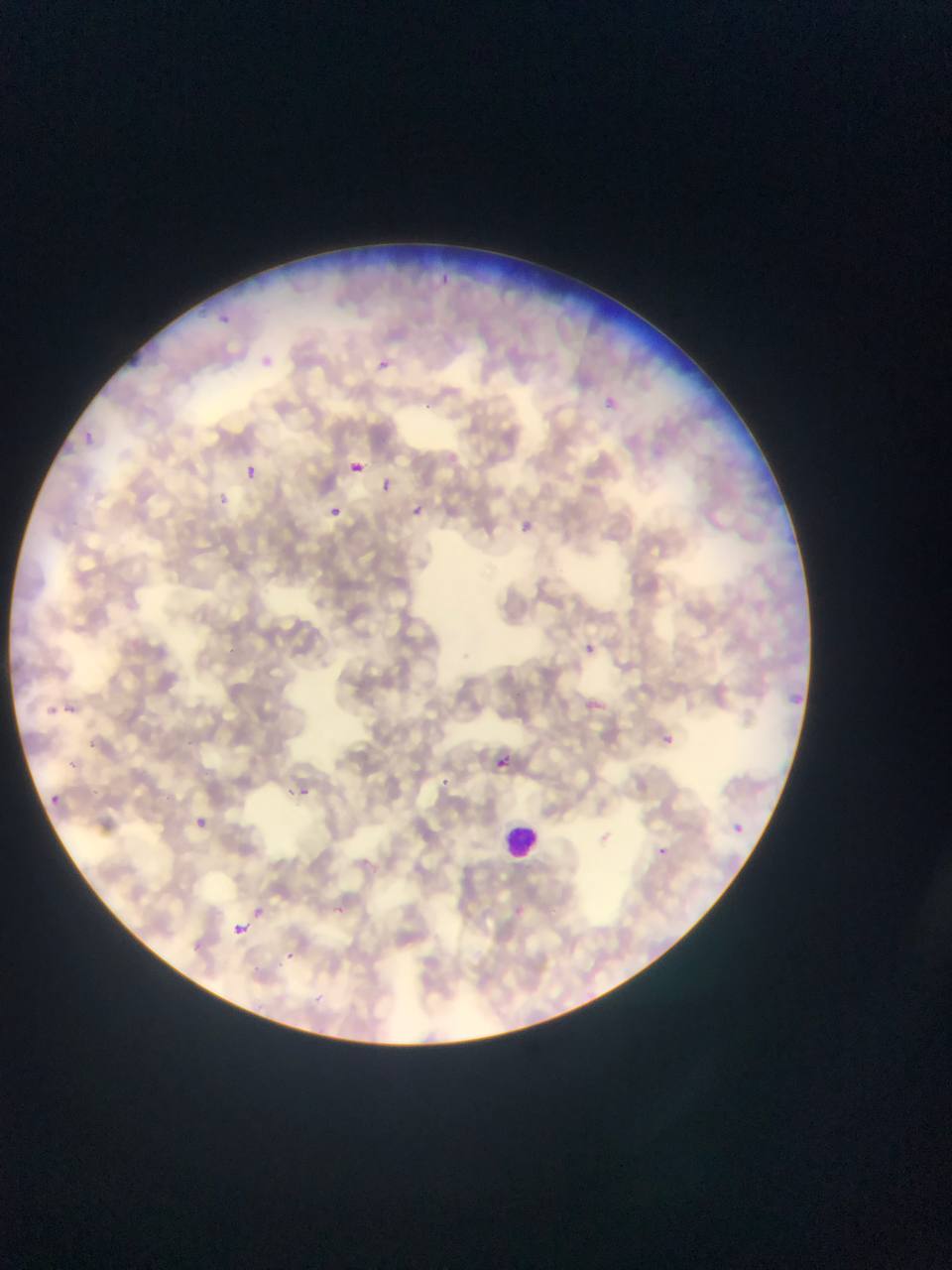
Approximate bounding boxes as (left, top, right, bottom) in pixels. Leukocyte locations: (499, 820, 535, 860). Malaria parasite locations: (426, 273, 462, 291), (219, 313, 230, 323), (258, 342, 298, 375), (126, 347, 149, 373), (377, 359, 390, 370), (600, 390, 617, 411), (83, 437, 91, 449), (345, 448, 362, 471), (245, 465, 258, 479), (375, 468, 403, 501), (202, 486, 233, 507), (400, 501, 440, 529), (509, 503, 540, 539), (331, 507, 340, 517), (577, 628, 600, 678), (785, 681, 808, 707), (48, 706, 58, 713), (650, 719, 693, 747), (497, 756, 508, 769), (438, 772, 476, 823), (289, 777, 327, 803), (51, 795, 60, 804), (179, 804, 227, 842), (722, 812, 753, 838), (653, 837, 681, 865), (324, 893, 364, 921), (248, 896, 284, 917), (226, 918, 247, 953), (266, 944, 297, 980). Single field of view. Image is 952×1270 pixels. Thin blood film. Sample from Ghana. Mobile-phone photograph taken through the microscope.